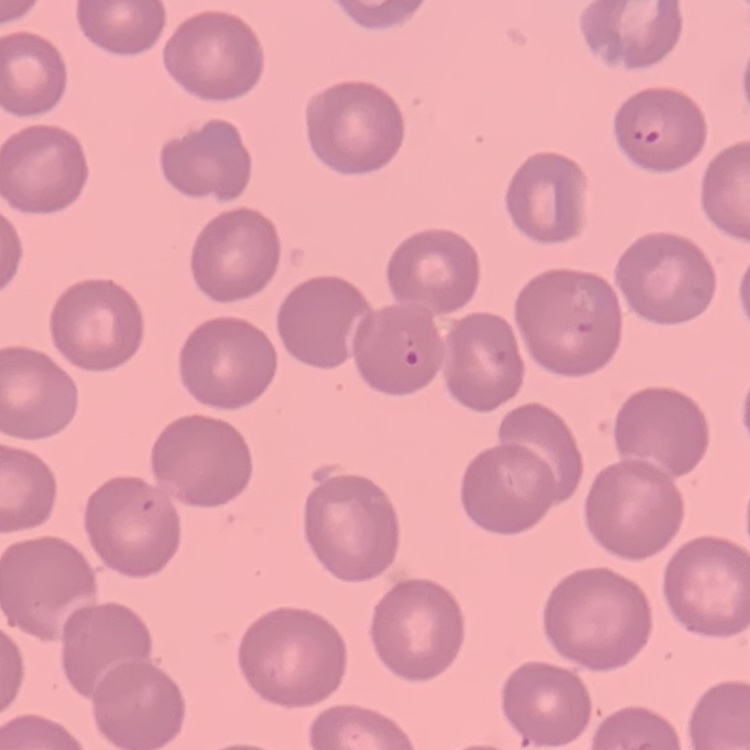 The red blood cells exhibit no rouleaux formation. Thin blood film. Stained with either Field's or Giemsa. One tile cut from a larger photomicrograph.